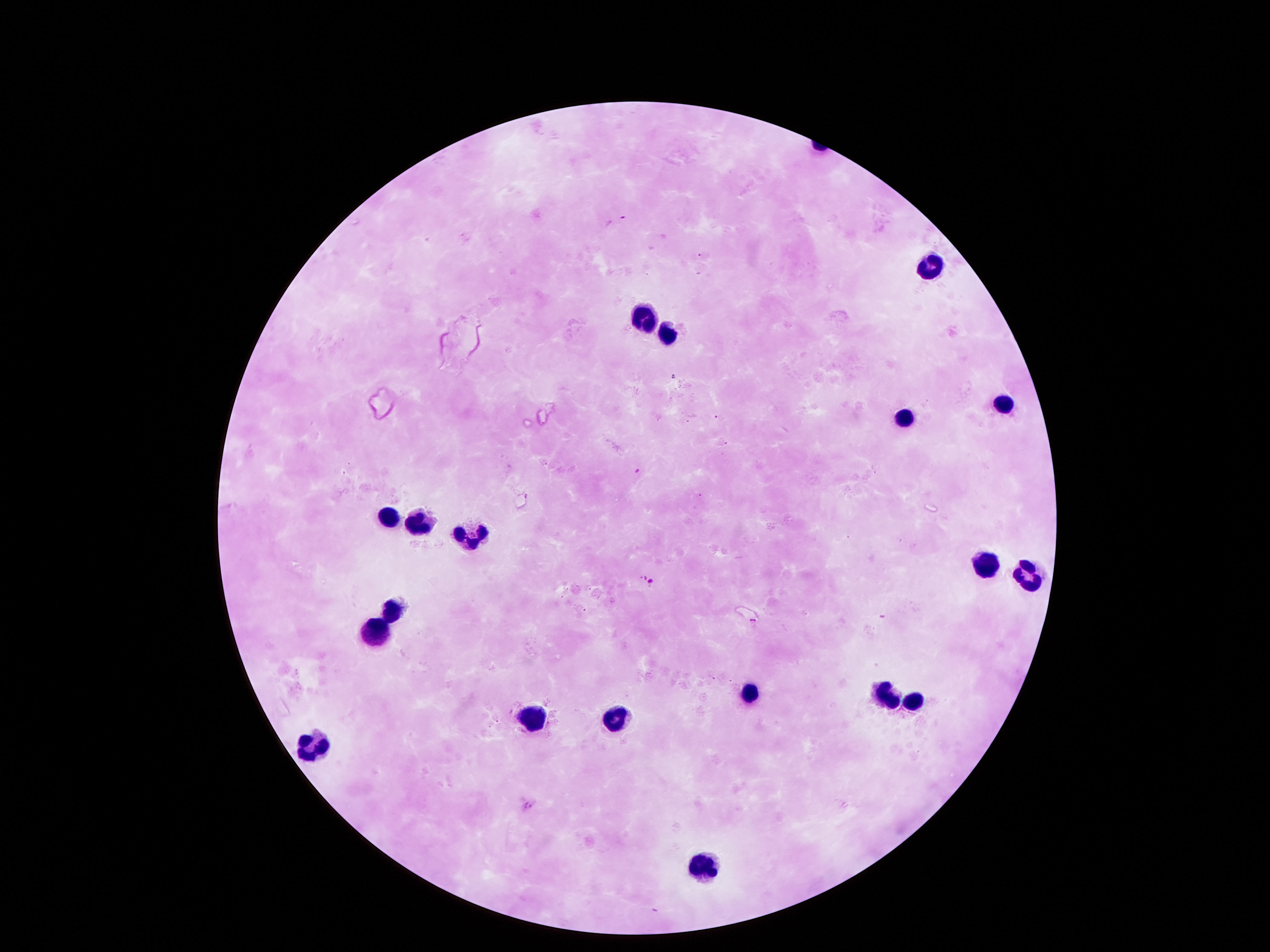 Approximate centers as {x, y} in pixels. Leukocyte locations: {931, 264}, {642, 311}, {669, 334}, {1005, 402}, {904, 412}, {383, 515}, {424, 523}, {471, 536}, {985, 563}, {1032, 576}, {390, 607}, {373, 629}, {750, 691}, {884, 694}, {911, 701}, {612, 710}, {528, 718}, {313, 744}, {703, 862}. 100x magnification. Patient malaria status: uninfected. Thick blood film. Giemsa-stained preparation. Image is 1270×952 pixels. Photographed through the microscope eyepiece with a smartphone camera. Single field of view.